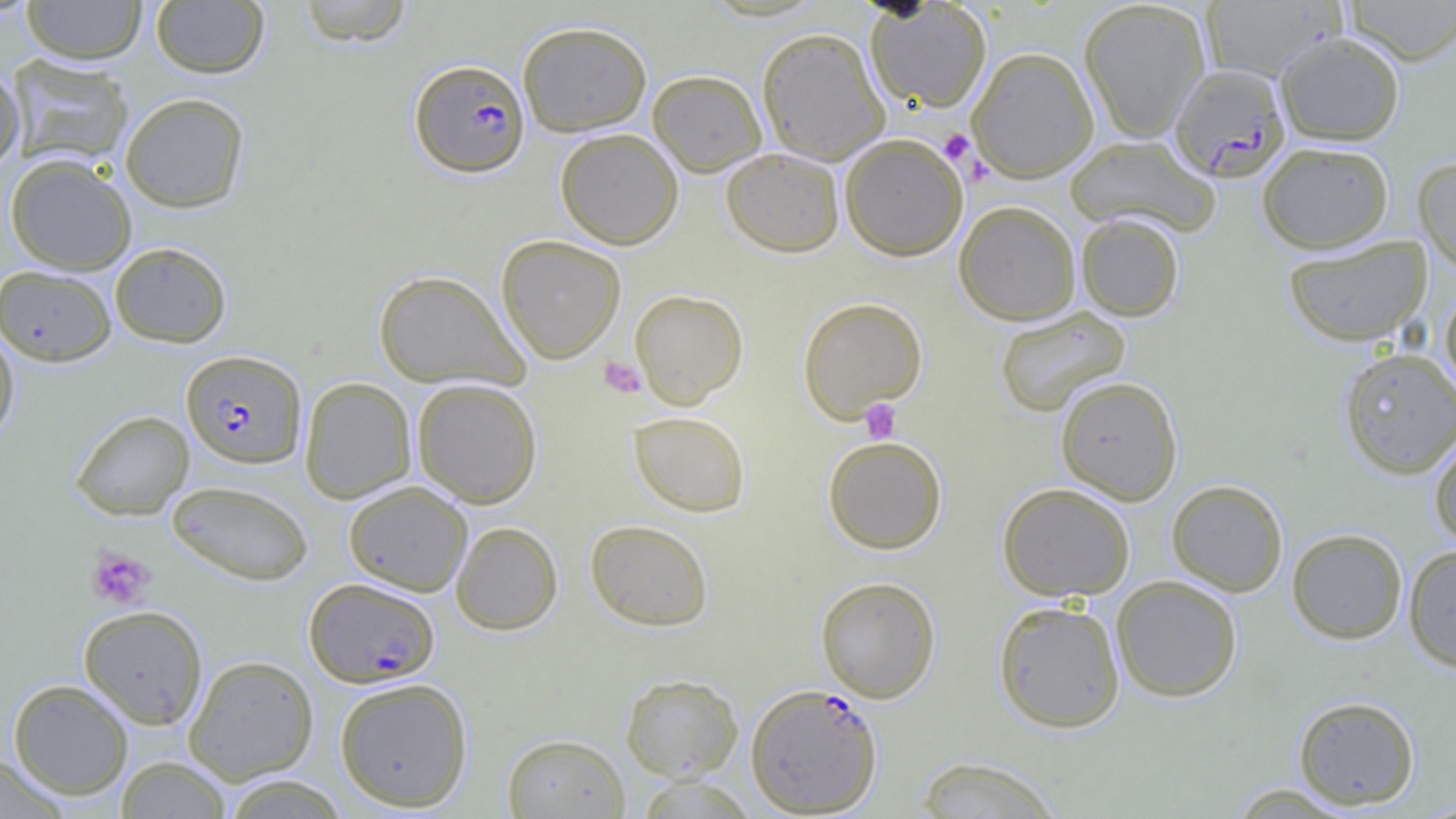

Approximate bounding boxes as named x1/y1/x2/y2 corners in pixels. Platelet locations: (x1=938, y1=129, x2=977, y2=167), (x1=598, y1=356, x2=646, y2=398), (x1=859, y1=399, x2=901, y2=443), (x1=86, y1=547, x2=156, y2=610). Uninfected red blood cell locations: (x1=22, y1=0, x2=147, y2=64), (x1=297, y1=0, x2=413, y2=48), (x1=1078, y1=0, x2=1211, y2=142), (x1=1345, y1=0, x2=1456, y2=64), (x1=150, y1=1, x2=270, y2=78), (x1=1200, y1=1, x2=1344, y2=81), (x1=866, y1=2, x2=991, y2=112), (x1=517, y1=20, x2=652, y2=137), (x1=756, y1=26, x2=890, y2=165), (x1=1275, y1=31, x2=1405, y2=145), (x1=967, y1=46, x2=1099, y2=182), (x1=7, y1=55, x2=133, y2=169), (x1=0, y1=64, x2=25, y2=170), (x1=648, y1=70, x2=767, y2=176), (x1=120, y1=92, x2=250, y2=213), (x1=555, y1=127, x2=684, y2=249), (x1=840, y1=133, x2=968, y2=261), (x1=1065, y1=135, x2=1219, y2=236), (x1=1257, y1=141, x2=1394, y2=254), (x1=722, y1=148, x2=844, y2=257), (x1=4, y1=154, x2=137, y2=274), (x1=1413, y1=156, x2=1456, y2=272), (x1=954, y1=200, x2=1081, y2=325), (x1=1076, y1=213, x2=1185, y2=321), (x1=496, y1=234, x2=626, y2=364), (x1=1282, y1=235, x2=1432, y2=347), (x1=109, y1=242, x2=231, y2=347), (x1=0, y1=264, x2=116, y2=366), (x1=372, y1=270, x2=529, y2=390), (x1=1439, y1=286, x2=1456, y2=399), (x1=629, y1=289, x2=749, y2=409), (x1=797, y1=296, x2=928, y2=422), (x1=994, y1=306, x2=1131, y2=417), (x1=0, y1=324, x2=20, y2=448), (x1=1339, y1=347, x2=1456, y2=480), (x1=1055, y1=375, x2=1183, y2=505), (x1=300, y1=377, x2=417, y2=504), (x1=412, y1=378, x2=543, y2=508), (x1=70, y1=410, x2=194, y2=521), (x1=628, y1=411, x2=751, y2=518), (x1=1428, y1=431, x2=1456, y2=548), (x1=822, y1=436, x2=947, y2=554), (x1=166, y1=479, x2=314, y2=585), (x1=1167, y1=479, x2=1288, y2=596), (x1=344, y1=480, x2=472, y2=596), (x1=997, y1=482, x2=1135, y2=601), (x1=584, y1=519, x2=714, y2=631), (x1=451, y1=521, x2=563, y2=635), (x1=1286, y1=528, x2=1408, y2=644), (x1=1403, y1=544, x2=1456, y2=673), (x1=1110, y1=575, x2=1242, y2=702), (x1=815, y1=576, x2=941, y2=702), (x1=993, y1=600, x2=1126, y2=733), (x1=78, y1=604, x2=208, y2=729), (x1=183, y1=655, x2=319, y2=784), (x1=619, y1=672, x2=744, y2=781), (x1=334, y1=676, x2=473, y2=811), (x1=8, y1=679, x2=133, y2=800), (x1=1292, y1=695, x2=1420, y2=810), (x1=502, y1=732, x2=629, y2=818), (x1=0, y1=753, x2=72, y2=819), (x1=114, y1=756, x2=233, y2=818), (x1=913, y1=756, x2=1065, y2=818), (x1=220, y1=774, x2=352, y2=818), (x1=635, y1=775, x2=759, y2=819), (x1=1223, y1=782, x2=1363, y2=818). Plasmodium falciparum-infected red blood cell locations: (x1=409, y1=58, x2=530, y2=177), (x1=1169, y1=63, x2=1291, y2=182), (x1=181, y1=350, x2=307, y2=469), (x1=304, y1=577, x2=440, y2=687), (x1=745, y1=682, x2=883, y2=817). Slide-level diagnosis: Plasmodium falciparum. Optical microscopy. Image is 1456×819 pixels. One field of a larger specimen. Captured at 1000x magnification. Thin blood smear.